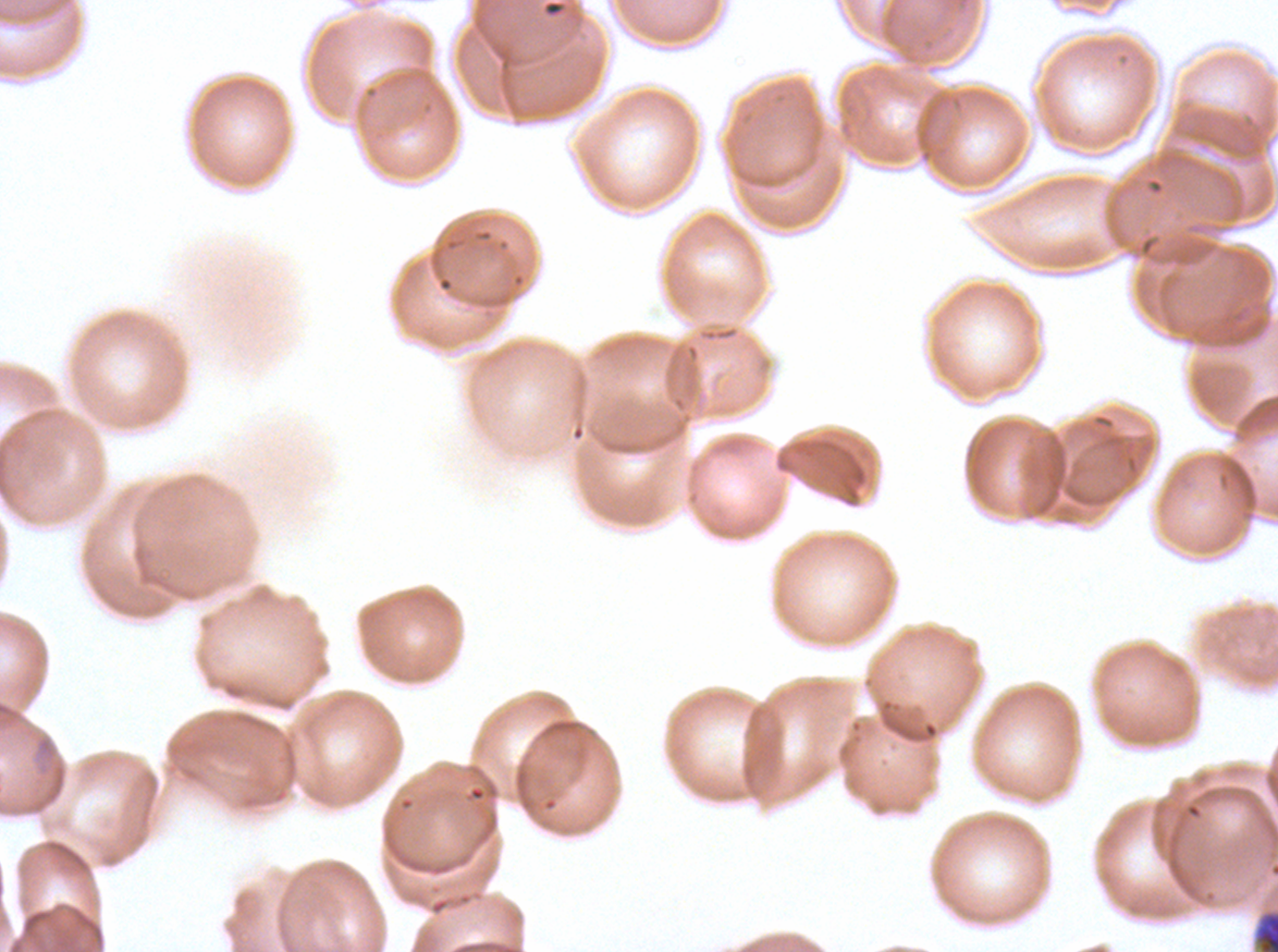
notation = approximate bounding boxes as (x1, y1, x2, y2) in pixels
early schizont locations = (1251, 907, 1277, 951)
field of view = sub-image separated from a larger composite
specimen = ex-vivo Plasmodium falciparum culture from a patient in The Gambia, grown for 24 to 48 hours
preparation = thin blood smear
image size = 1278×952 pixels
stain = Giemsa